Assess this cell for malaria.
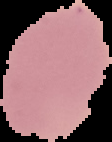

Uninfected.

Image is 112×142 pixels. From a thin blood film. The area outside the segmented cell region is set to black.